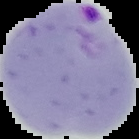
preparation = thin blood smear
malaria status = parasitized
image type = cell region segmented out of the field of view; surrounding area masked to black
image size = 139×139 pixels